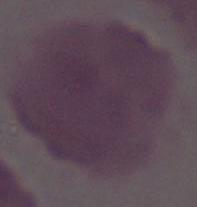
magnification = 1000x
modality = photomicrograph
identification = red blood cell